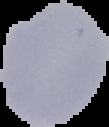
image type = segmented cell region with the area outside set to black
preparation = thin blood film
image size = 109×127 pixels
result = negative for malaria parasites